Classify this cell by malaria status.
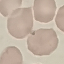
Uninfected.

Summary:
  - Preparation: thin smear
  - Image type: automatically extracted cell patch, resized to 64 × 64 pixels
  - Stain: Giemsa
  - Capture: smartphone through the microscope eyepiece